Locate platelets.
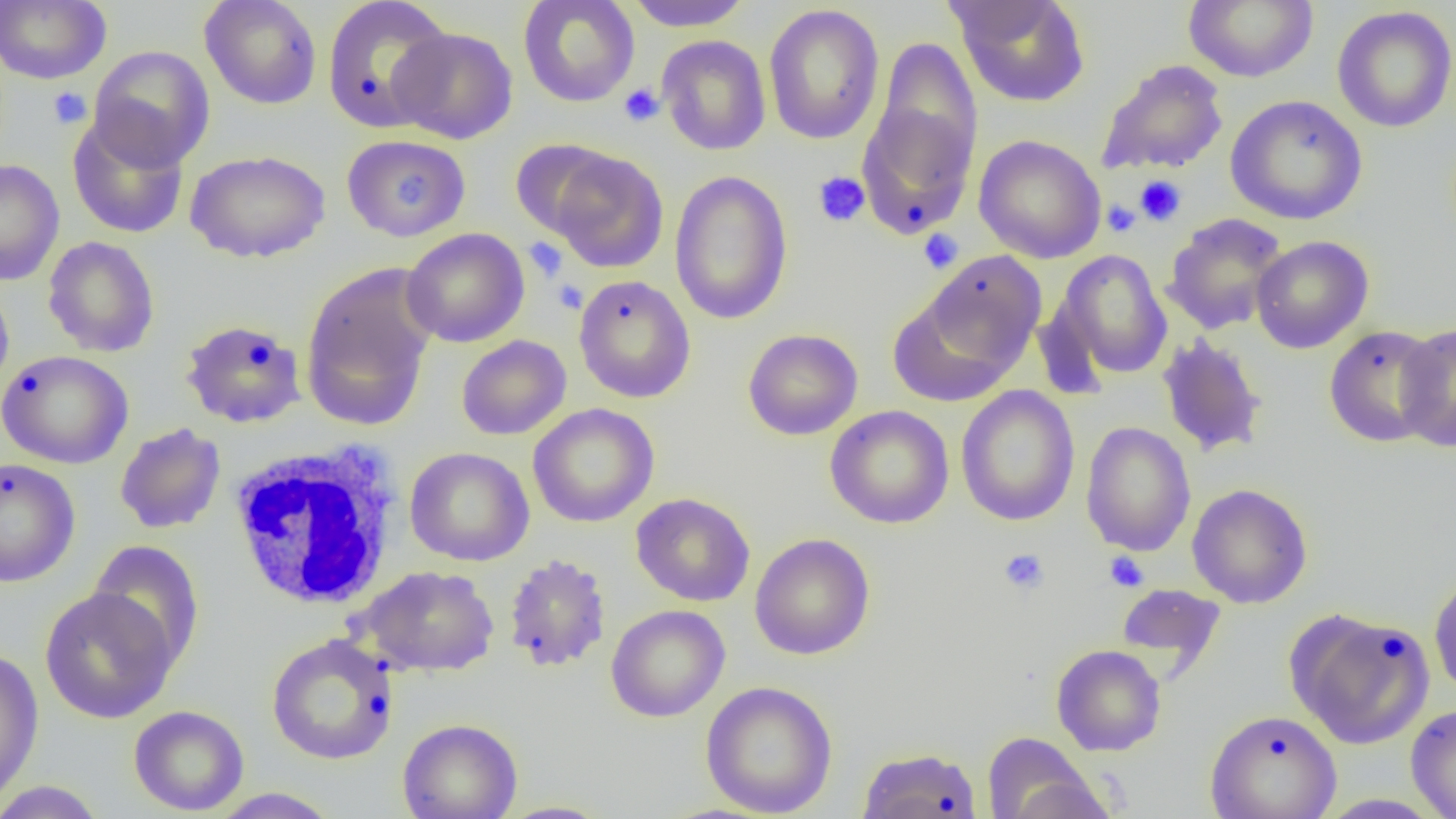

Approximate bounding boxes as [x1, y1, x2, y2] in pixels.
Platelets: [618, 83, 665, 127], [48, 87, 92, 129], [813, 171, 871, 228], [394, 172, 430, 210], [1134, 175, 1186, 226], [1101, 199, 1141, 238], [918, 229, 963, 273], [524, 237, 568, 282], [553, 279, 587, 313], [998, 548, 1049, 595], [1104, 551, 1149, 592].

Uninfected red blood cell locations: [199, 0, 322, 110], [321, 0, 453, 133], [518, 0, 640, 108], [624, 0, 754, 31], [953, 0, 1091, 108], [1183, 0, 1319, 83], [0, 1, 111, 84], [763, 5, 886, 145], [1332, 5, 1456, 133], [388, 26, 519, 144], [657, 35, 771, 156], [871, 36, 983, 176], [88, 45, 215, 170], [1096, 58, 1229, 176], [1226, 95, 1367, 225], [856, 99, 978, 238], [68, 112, 190, 239], [341, 134, 470, 242], [973, 134, 1106, 263], [509, 140, 620, 240], [548, 149, 668, 273], [185, 150, 330, 263], [0, 159, 65, 286], [669, 170, 794, 325], [1162, 214, 1288, 335], [402, 227, 530, 348], [1250, 235, 1374, 354], [42, 236, 160, 358], [1055, 249, 1173, 382], [920, 252, 1047, 377], [300, 265, 437, 432], [573, 274, 696, 403], [0, 278, 15, 400], [886, 288, 1026, 406], [180, 319, 307, 428], [1394, 322, 1456, 452], [1323, 325, 1444, 448], [742, 328, 863, 440], [1156, 333, 1269, 458], [456, 335, 571, 440], [0, 350, 134, 469], [955, 385, 1081, 527], [528, 403, 659, 528], [825, 405, 954, 529], [1081, 421, 1196, 557], [114, 423, 226, 534], [405, 447, 534, 566], [0, 457, 81, 587], [1187, 483, 1313, 608], [631, 492, 756, 607], [749, 533, 876, 660], [87, 541, 205, 671], [502, 553, 612, 674], [357, 565, 500, 677], [1429, 572, 1456, 698], [1116, 583, 1226, 673], [39, 587, 179, 723], [606, 604, 730, 722], [1286, 609, 1435, 750], [266, 634, 399, 766], [1051, 644, 1166, 756], [0, 648, 44, 808], [700, 680, 838, 817], [1406, 704, 1456, 819], [128, 705, 249, 816], [1205, 709, 1342, 819], [397, 718, 523, 819], [982, 732, 1108, 819], [856, 746, 982, 819], [0, 780, 109, 818], [206, 788, 343, 818], [1314, 793, 1447, 818], [492, 801, 616, 819]. White blood cell locations: [227, 440, 404, 611]. Slide-level diagnosis: negative for blood parasites. Single field of view. 1000x magnification. Image is 1456×819 pixels. Thin blood film. Light microscopy.